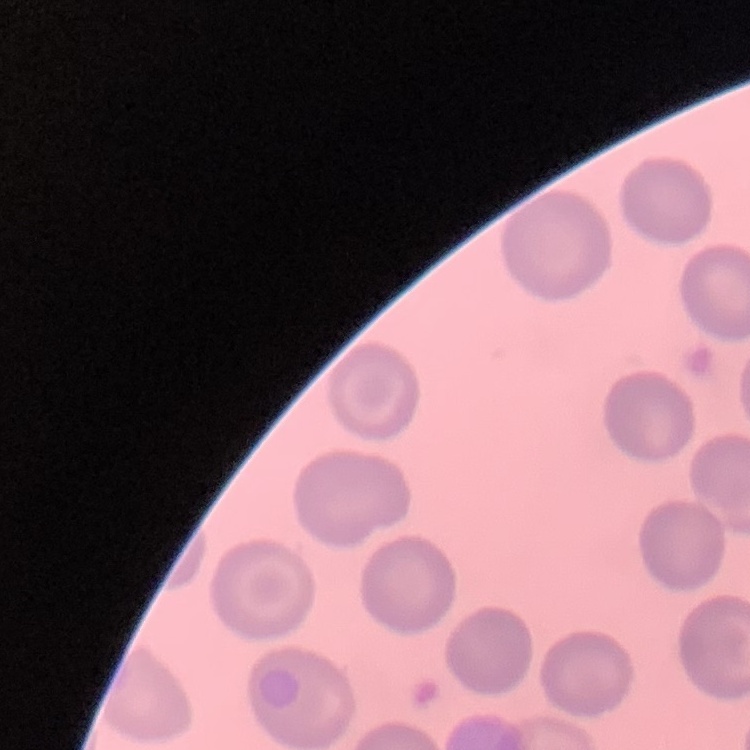
red blood cell morphology = no rouleaux formation
preparation = thin peripheral smear
stain = Field's or Giemsa
image type = one tile cut from a larger photomicrograph